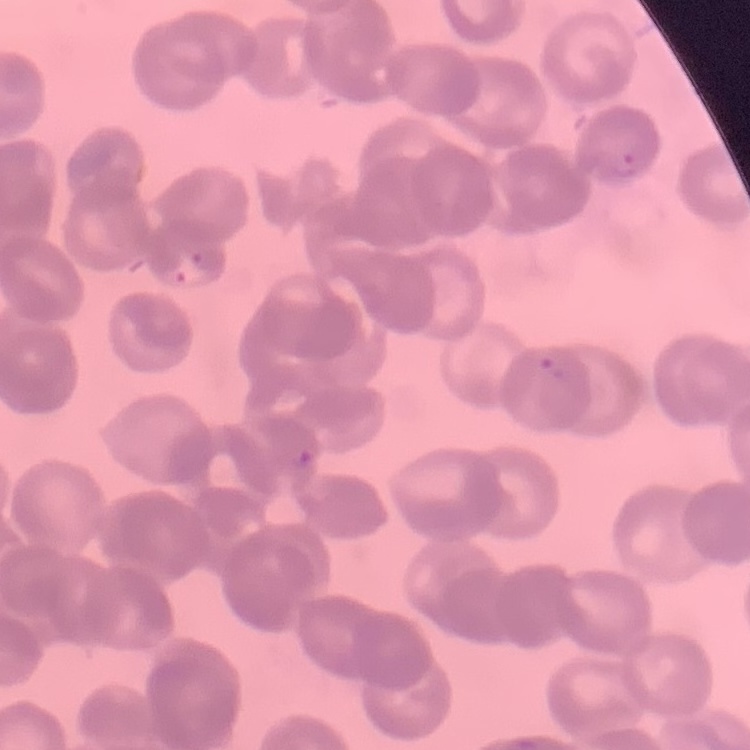
{
  "erythrocyte_morphology": "rouleaux formation",
  "stain": "Field's or Giemsa",
  "preparation": "thin blood smear",
  "image_type": "square crop of a larger photomicrograph"
}